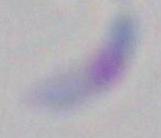
Summary:
  - Identification: Toxoplasma gondii
  - Magnification: 1000x
  - Modality: photomicrograph